Name the blood parasite species.
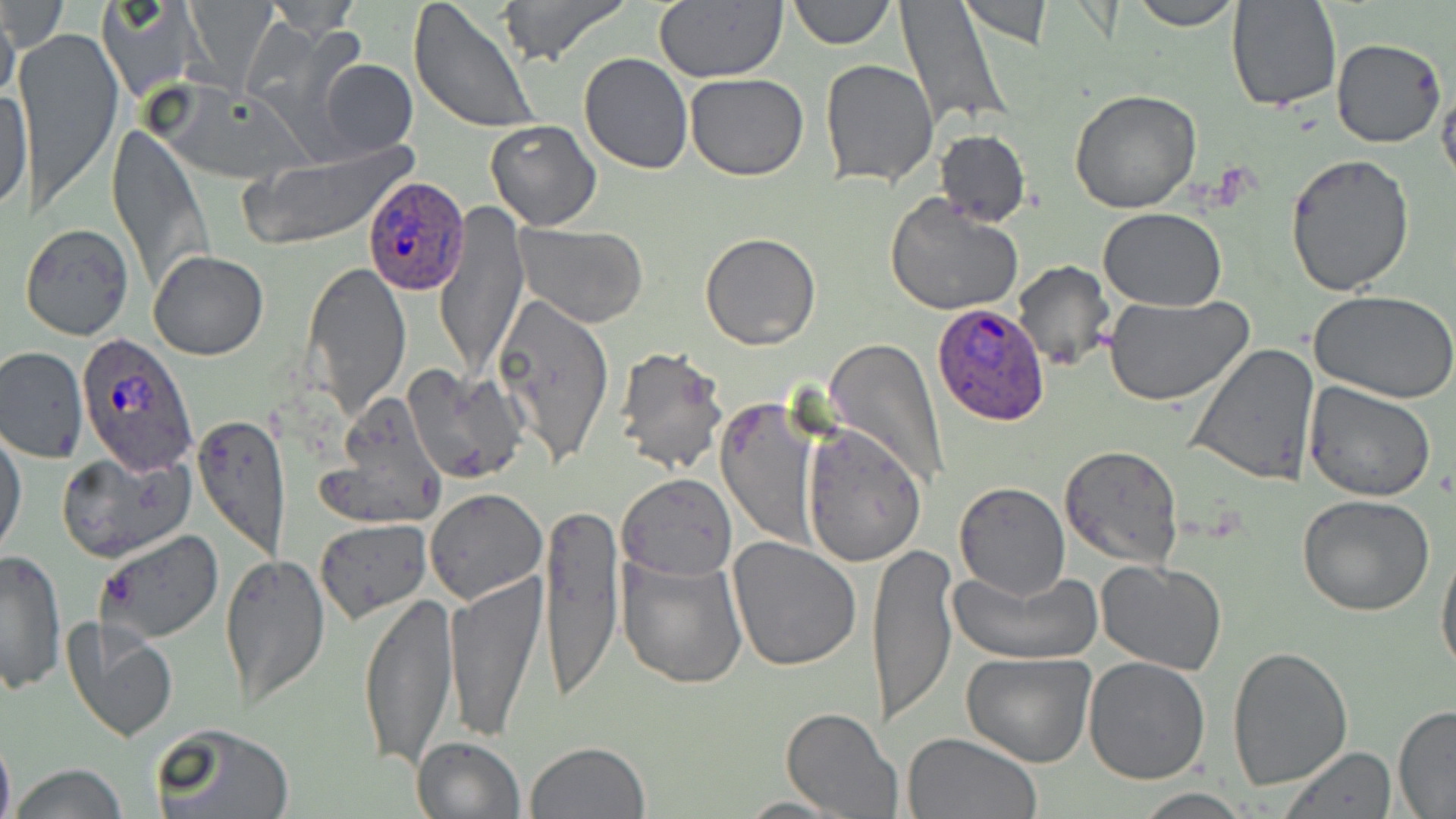
Plasmodium ovale.

field_of_view: one of a larger specimen
plasmodium_ovale_infected_red_blood_cell_locations: 'approximate bounding boxes as named x1/y1/x2/y2 corners in pixels: (x1=363, y1=177, x2=471, y2=295), (x1=932, y1=300, x2=1051, y2=425), (x1=74, y1=335, x2=199, y2=479)'
preparation: thin blood smear
stain: May-Grünwald-Giemsa
modality: optical microscopy
image_size: 1456×819 pixels
magnification: 1000x
uninfected_red_blood_cell_locations: 'approximate bounding boxes as named x1/y1/x2/y2 corners in pixels: (x1=2, y1=0, x2=67, y2=54), (x1=5, y1=0, x2=36, y2=86), (x1=98, y1=0, x2=204, y2=102), (x1=408, y1=0, x2=541, y2=135), (x1=498, y1=0, x2=630, y2=66), (x1=654, y1=0, x2=787, y2=83), (x1=787, y1=0, x2=894, y2=48), (x1=899, y1=0, x2=1012, y2=130), (x1=961, y1=0, x2=1053, y2=46), (x1=1128, y1=0, x2=1243, y2=29), (x1=260, y1=1, x2=367, y2=34), (x1=1226, y1=1, x2=1342, y2=114), (x1=0, y1=7, x2=20, y2=113), (x1=16, y1=29, x2=124, y2=211), (x1=1331, y1=37, x2=1446, y2=149), (x1=578, y1=53, x2=692, y2=174), (x1=318, y1=58, x2=417, y2=157), (x1=821, y1=60, x2=938, y2=187), (x1=685, y1=72, x2=810, y2=180), (x1=1435, y1=73, x2=1456, y2=188), (x1=0, y1=80, x2=31, y2=217), (x1=1069, y1=88, x2=1202, y2=211), (x1=485, y1=120, x2=601, y2=232), (x1=107, y1=125, x2=210, y2=292), (x1=934, y1=128, x2=1030, y2=228), (x1=242, y1=146, x2=410, y2=248), (x1=1284, y1=153, x2=1415, y2=296), (x1=886, y1=193, x2=1023, y2=317), (x1=436, y1=203, x2=529, y2=380), (x1=1097, y1=208, x2=1226, y2=311), (x1=22, y1=223, x2=134, y2=341), (x1=513, y1=223, x2=650, y2=329), (x1=700, y1=233, x2=820, y2=350), (x1=148, y1=250, x2=269, y2=360), (x1=1012, y1=260, x2=1113, y2=372), (x1=302, y1=263, x2=413, y2=420), (x1=1309, y1=291, x2=1456, y2=405), (x1=1102, y1=294, x2=1255, y2=407), (x1=491, y1=295, x2=614, y2=466), (x1=826, y1=340, x2=948, y2=492), (x1=1188, y1=343, x2=1321, y2=486), (x1=0, y1=345, x2=87, y2=462), (x1=611, y1=346, x2=729, y2=475), (x1=403, y1=364, x2=527, y2=483), (x1=1303, y1=381, x2=1437, y2=502), (x1=718, y1=398, x2=820, y2=548), (x1=321, y1=401, x2=446, y2=528), (x1=193, y1=414, x2=292, y2=559), (x1=802, y1=423, x2=928, y2=568), (x1=1, y1=430, x2=27, y2=562), (x1=1060, y1=445, x2=1183, y2=569), (x1=59, y1=449, x2=196, y2=562), (x1=617, y1=473, x2=737, y2=580), (x1=954, y1=482, x2=1070, y2=600), (x1=423, y1=489, x2=546, y2=606), (x1=1297, y1=494, x2=1435, y2=616), (x1=537, y1=497, x2=622, y2=704), (x1=315, y1=518, x2=433, y2=622), (x1=94, y1=527, x2=225, y2=644), (x1=726, y1=536, x2=862, y2=670), (x1=1436, y1=539, x2=1456, y2=679), (x1=869, y1=543, x2=956, y2=725), (x1=1, y1=549, x2=67, y2=694), (x1=219, y1=551, x2=331, y2=711), (x1=618, y1=553, x2=748, y2=686), (x1=1096, y1=559, x2=1226, y2=675), (x1=957, y1=569, x2=1097, y2=665), (x1=443, y1=571, x2=546, y2=742), (x1=359, y1=590, x2=460, y2=770), (x1=60, y1=617, x2=176, y2=741), (x1=1227, y1=646, x2=1353, y2=790), (x1=961, y1=651, x2=1096, y2=767), (x1=1083, y1=656, x2=1210, y2=785), (x1=1392, y1=705, x2=1456, y2=816), (x1=782, y1=707, x2=903, y2=817), (x1=151, y1=723, x2=294, y2=819), (x1=0, y1=729, x2=14, y2=819), (x1=901, y1=731, x2=1042, y2=818), (x1=411, y1=736, x2=526, y2=819), (x1=523, y1=739, x2=652, y2=819), (x1=1279, y1=746, x2=1398, y2=818), (x1=8, y1=764, x2=129, y2=819), (x1=1135, y1=790, x2=1253, y2=819), (x1=734, y1=795, x2=850, y2=817)'